Outline each blood parasite and name the species.
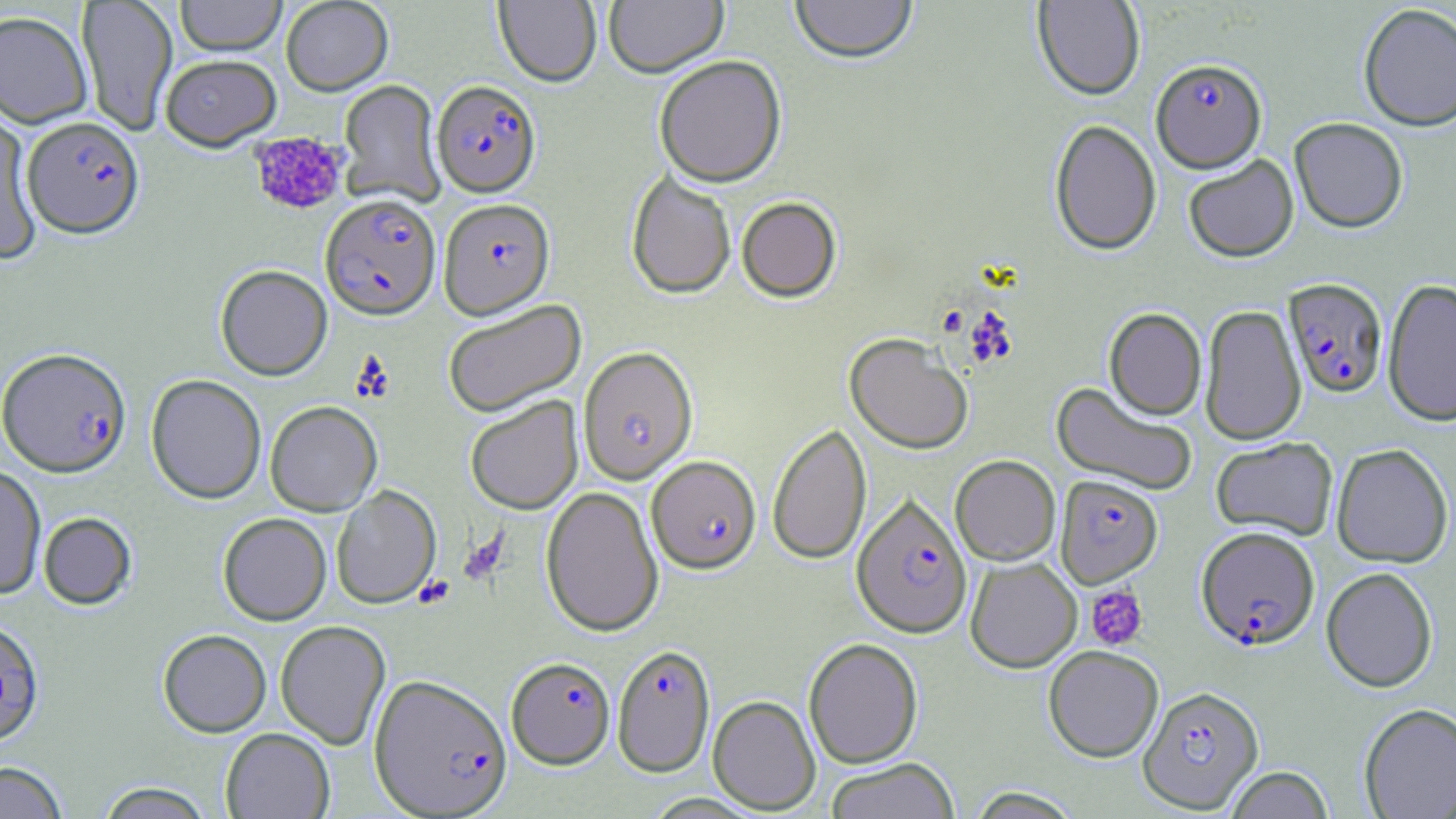
Approximate bounding boxes as [x1, y1, x2, y2] in pixels.
Plasmodium falciparum-infected red blood cells: [1151, 58, 1267, 173], [432, 80, 542, 197], [23, 116, 144, 238], [320, 194, 441, 321], [439, 198, 555, 319], [1283, 278, 1388, 398], [577, 346, 698, 485], [0, 348, 131, 477], [642, 450, 757, 568], [1055, 475, 1163, 587], [839, 495, 960, 640], [1196, 526, 1320, 650], [612, 643, 715, 777], [506, 657, 615, 769], [368, 673, 513, 817], [1138, 685, 1264, 813].
No Plasmodium ovale, Plasmodium malariae, Plasmodium vivax, Babesia divergens, or Trypanosoma brucei observed.

slide-level diagnosis = Plasmodium falciparum
magnification = 1000x
field of view = one of a larger specimen
image size = 1456×819 pixels
platelet locations = approximate bounding boxes as [x1, y1, x2, y2] in pixels: [249, 131, 348, 215], [458, 531, 508, 586], [414, 575, 455, 610], [1086, 585, 1149, 650]
stain = May-Grünwald-Giemsa
uninfected red blood cell locations = approximate bounding boxes as [x1, y1, x2, y2] in pixels: [175, 0, 286, 57], [281, 0, 393, 96], [494, 0, 601, 87], [604, 0, 728, 78], [790, 0, 917, 65], [1032, 0, 1145, 101], [77, 1, 177, 136], [1358, 3, 1456, 132], [0, 11, 92, 129], [161, 55, 281, 150], [654, 55, 787, 187], [339, 80, 444, 207], [0, 110, 43, 265], [1289, 117, 1408, 233], [1049, 119, 1162, 255], [1183, 155, 1299, 262], [626, 170, 736, 299], [737, 196, 842, 302], [216, 265, 332, 380], [1383, 277, 1456, 426], [442, 299, 586, 417], [1200, 305, 1306, 446], [1104, 308, 1206, 420], [845, 333, 973, 454], [146, 374, 266, 504], [1051, 382, 1198, 496], [465, 396, 583, 514], [265, 401, 382, 515], [767, 422, 872, 565], [1211, 437, 1338, 540], [1331, 443, 1453, 567], [950, 455, 1060, 565], [0, 465, 46, 599], [332, 486, 441, 608], [541, 486, 664, 636], [39, 512, 136, 609], [218, 513, 331, 625], [965, 557, 1082, 672], [1321, 567, 1438, 692], [0, 619, 44, 745], [275, 620, 391, 749], [158, 629, 271, 737], [803, 637, 923, 769], [1043, 646, 1163, 762], [708, 695, 821, 814], [1358, 703, 1456, 819], [220, 728, 335, 818], [825, 758, 960, 819], [0, 761, 69, 819], [1225, 766, 1333, 818], [94, 782, 216, 819], [965, 787, 1083, 819]
modality = optical microscopy
preparation = thin blood film